Comment on the morphology of the red blood cells.
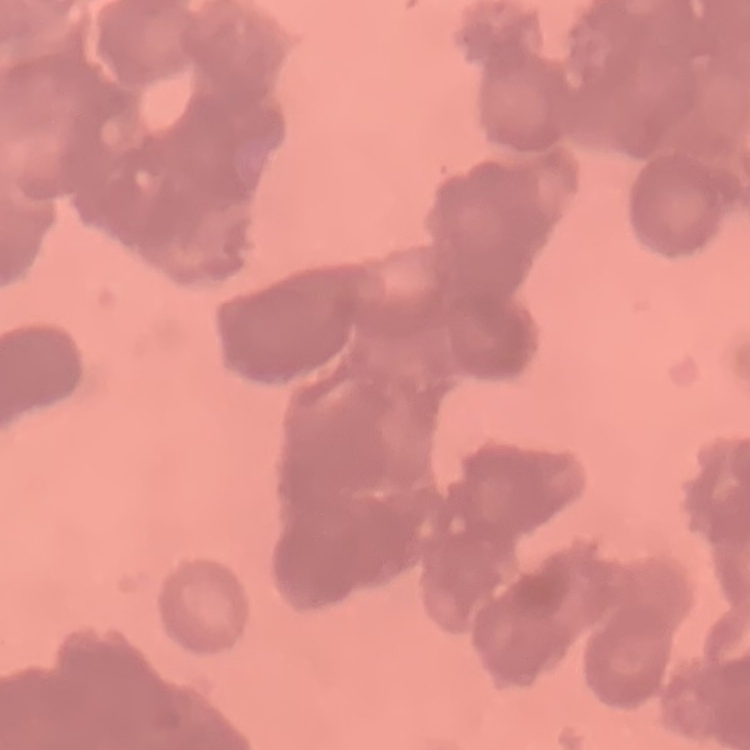
They show rouleaux formation.

One tile cut from a larger photomicrograph. Thin peripheral smear. Stained with either Field's or Giemsa.